State which cell type is depicted.
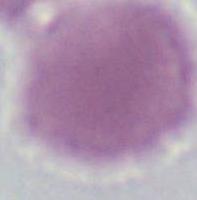

This is an erythrocyte.

Micrograph. Captured at 1000x magnification.